Outline each blood parasite and name the species.
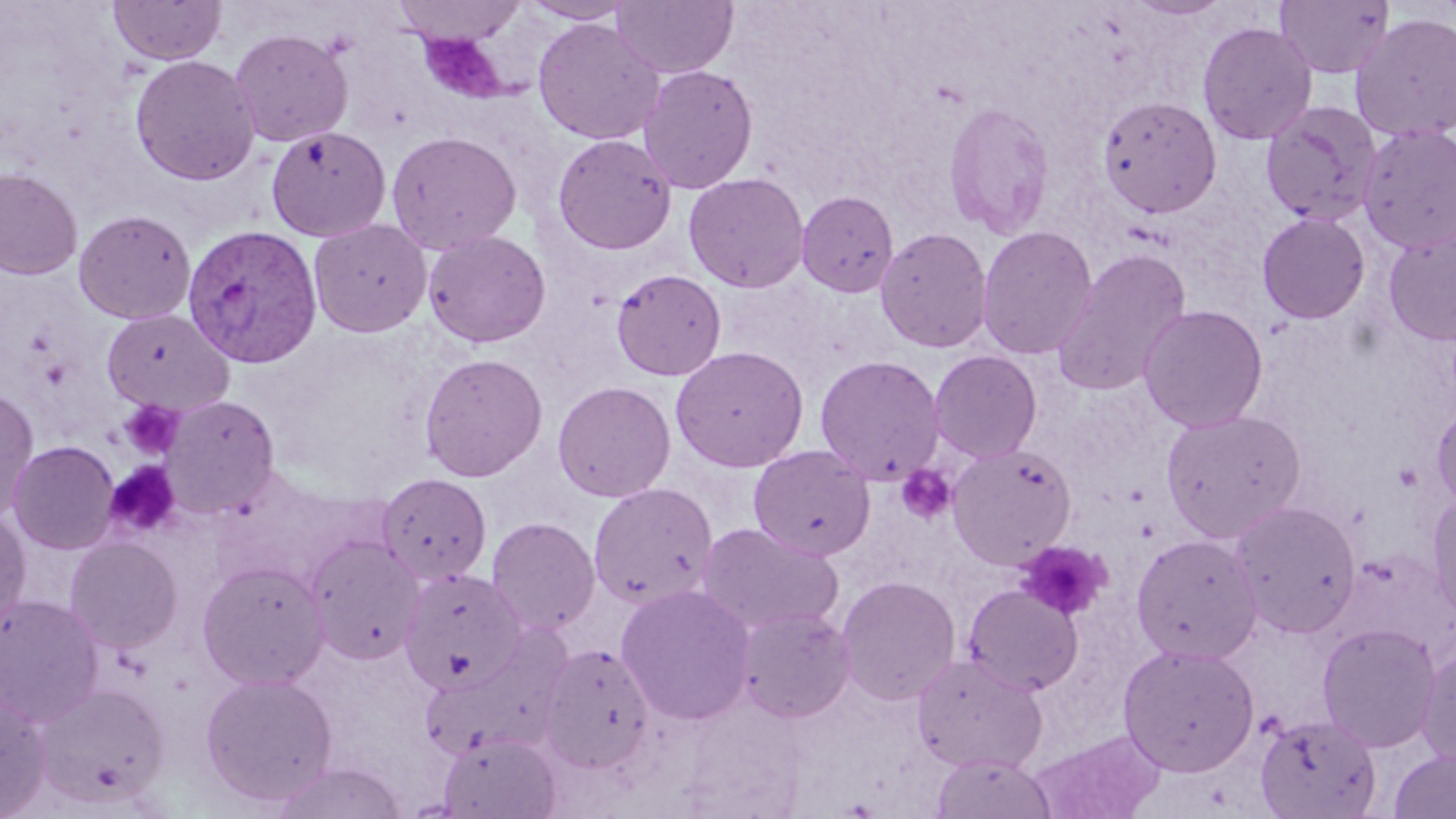

Approximate bounding boxes as (x1,y1)-(x2,y2) corner pairs in pixels.
Plasmodium vivax-infected red blood cells: (181,223)-(323,369).
No Plasmodium falciparum, Plasmodium ovale, Plasmodium malariae, Babesia divergens, or Trypanosoma brucei observed.

Summary:
  - Platelet locations (subset): (420,33)-(508,104), (119,401)-(184,460), (1393,462)-(1424,492), (895,464)-(957,525), (1014,541)-(1110,621)
  - Uninfected red blood cell locations (subset): (109,0)-(226,66), (391,0)-(526,47), (518,0)-(638,24), (611,0)-(738,79), (1124,0)-(1231,21), (1274,0)-(1395,78), (1350,13)-(1456,142), (532,18)-(664,145), (1197,21)-(1317,144), (229,27)-(353,147), (130,54)-(261,186), (637,64)-(759,194), (1097,94)-(1223,219), (943,101)-(1055,239), (1260,101)-(1382,226), (1358,123)-(1456,255), (266,126)-(391,242), (385,131)-(522,254), (552,133)-(677,254), (0,167)-(83,280), (684,172)-(809,293), (796,190)-(899,297), (74,209)-(196,325), (1257,212)-(1371,324), (308,218)-(432,337), (976,225)-(1098,361), (874,226)-(993,353), (423,228)-(551,348), (1384,229)-(1456,347), (1051,248)-(1192,397), (611,269)-(727,381), (1137,304)-(1268,433), (101,308)-(233,415), (670,345)-(809,472), (928,350)-(1043,463), (419,352)-(548,482), (814,354)-(945,485), (419,369)-(677,488), (552,380)-(676,502), (0,388)-(40,522), (161,395)-(280,518), (1431,407)-(1456,510), (1160,408)-(1306,542), (8,440)-(120,555), (946,443)-(1077,568), (748,445)-(876,561), (376,472)-(491,584), (588,482)-(718,610), (1427,492)-(1456,622), (1228,500)-(1362,638), (0,511)-(31,631), (486,517)-(601,636), (695,522)-(843,635), (1131,533)-(1263,664), (305,536)-(425,664), (65,538)-(182,653), (197,560)-(330,689), (399,567)-(526,694), (836,575)-(961,705), (616,583)-(757,725), (963,584)-(1084,695), (0,594)-(104,726), (736,606)-(855,723), (1317,623)-(1441,752), (419,628)-(575,763), (1417,642)-(1456,774), (1117,643)-(1260,776), (539,644)-(655,772), (911,655)-(1048,773), (200,672)-(338,806), (33,682)-(170,810), (0,693)-(52,818), (1254,713)-(1382,819), (1033,730)-(1165,819), (438,731)-(561,819), (1388,749)-(1456,818), (930,752)-(1058,819), (271,762)-(408,819)
  - Slide-level diagnosis: Plasmodium vivax
  - Field of view: single
  - Image size: 1456×819 pixels
  - Magnification: 1000x
  - Stain: May-Grünwald-Giemsa
  - Preparation: thin blood smear
  - Modality: optical microscopy